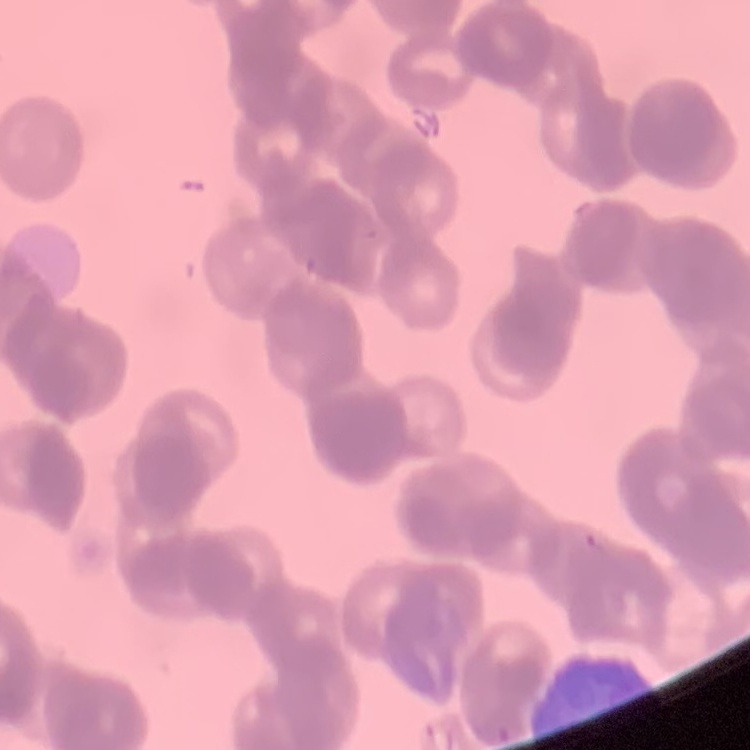

Summary:
  - Red blood cell morphology: rouleaux formation
  - Stain: Field's or Giemsa
  - Preparation: thin peripheral smear
  - Image type: one tile cut from a larger photomicrograph